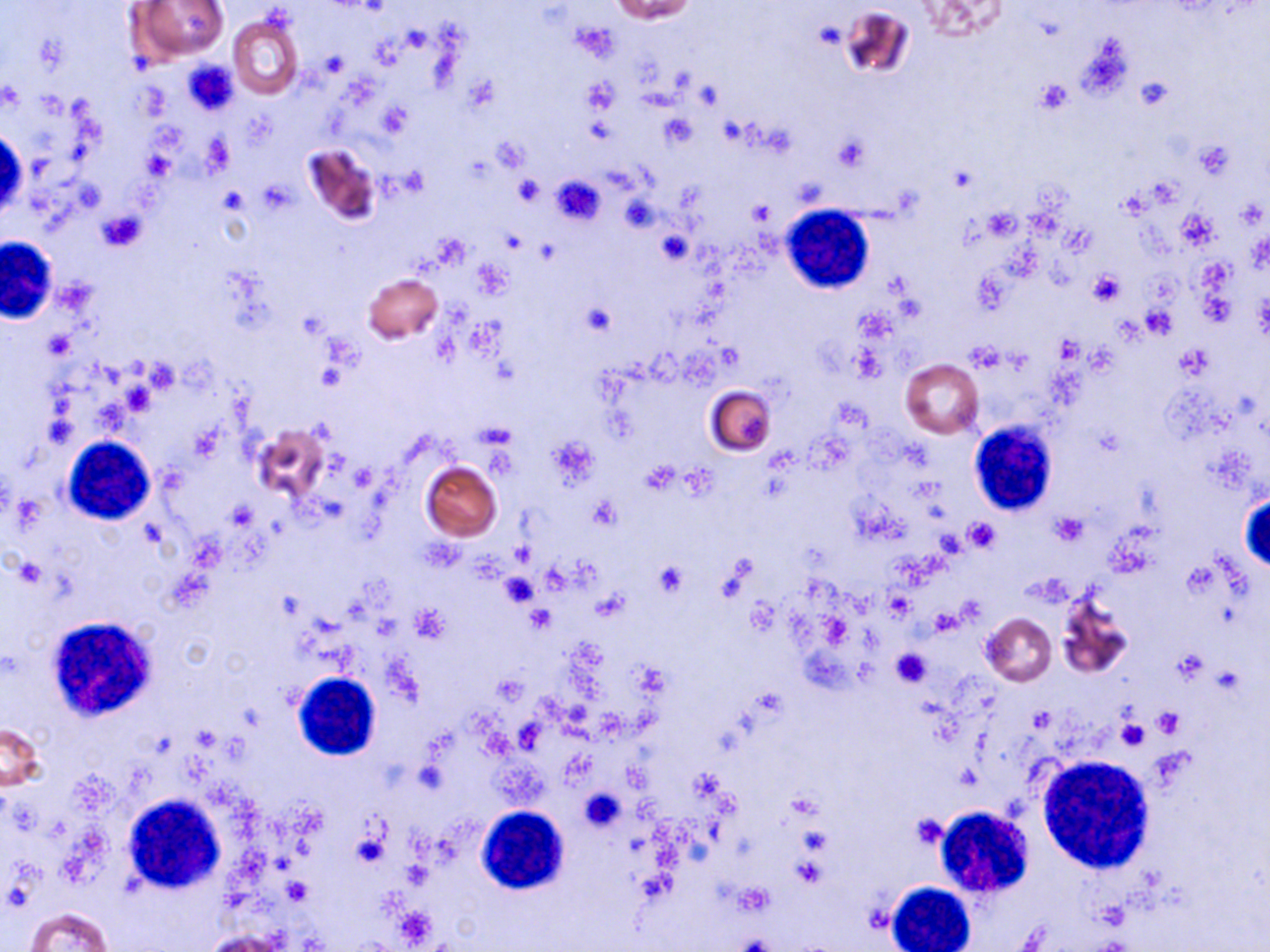
Summary:
  - Coordinate format: approximate bounding boxes as (x1,y1)-(x2,y2) corner pairs in pixels
  - White blood cell locations: (1,128)-(24,224), (783,205)-(873,294), (0,236)-(57,323), (969,424)-(1055,517), (62,436)-(156,525), (1240,493)-(1269,573), (58,621)-(159,725), (292,672)-(381,761), (1037,756)-(1155,874), (124,795)-(225,892), (477,807)-(568,894), (933,807)-(1032,899), (886,882)-(976,952)
  - Uninfected red blood cell locations: (610,0)-(698,22), (923,0)-(1006,41), (128,1)-(230,65), (839,8)-(913,80), (227,14)-(303,100), (302,144)-(380,225), (364,273)-(443,344), (900,359)-(983,439), (705,385)-(776,456), (251,423)-(329,503), (421,460)-(503,541), (1056,592)-(1134,679), (981,613)-(1056,686), (1,724)-(46,792), (26,907)-(111,952), (205,930)-(288,952)
  - Platelet locations: (574,23)-(619,61), (321,51)-(348,78), (182,58)-(238,116), (466,77)-(499,114), (1135,77)-(1174,112), (582,78)-(619,114), (1035,81)-(1071,114), (377,102)-(411,136), (660,114)-(698,148), (202,133)-(233,173), (495,136)-(529,172), (835,136)-(869,170), (1197,142)-(1231,177), (514,174)-(543,206), (551,175)-(605,227), (1118,191)-(1147,218), (621,194)-(658,232), (748,199)-(774,224), (97,210)-(146,251), (657,231)-(691,264), (1089,271)-(1124,305), (582,302)-(616,336), (1142,306)-(1176,339), (45,331)-(75,358), (967,341)-(1006,372), (850,344)-(887,381), (588,497)-(621,529), (227,500)-(257,530), (1051,512)-(1088,544), (964,518)-(1000,552), (653,562)-(687,597), (499,574)-(539,607), (413,606)-(450,641), (527,606)-(555,632), (892,648)-(931,686), (495,677)-(526,702), (1155,709)-(1185,735), (1116,718)-(1149,751), (788,792)-(820,817), (910,813)-(949,849), (350,830)-(390,869), (283,878)-(312,905)
  - Slide-level diagnosis: negative for blood parasites
  - Field of view: single
  - Modality: optical microscopy
  - Magnification: 1000x
  - Preparation: thin blood smear
  - Image size: 1270×952 pixels
  - Stain: May-Grünwald-Giemsa